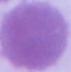
Summary:
  - Modality: photomicrograph
  - Magnification: 1000x
  - Identification: erythrocyte